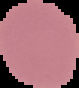
Malaria status: uninfected. From a thin blood film. Segmented cell region on a black background. Image is 79×88 pixels.